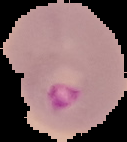

{
  "image_size": "127×142 pixels",
  "result": "malaria parasites detected",
  "preparation": "thin blood smear",
  "image_type": "cell region segmented out of the field of view; surrounding area masked to black"
}